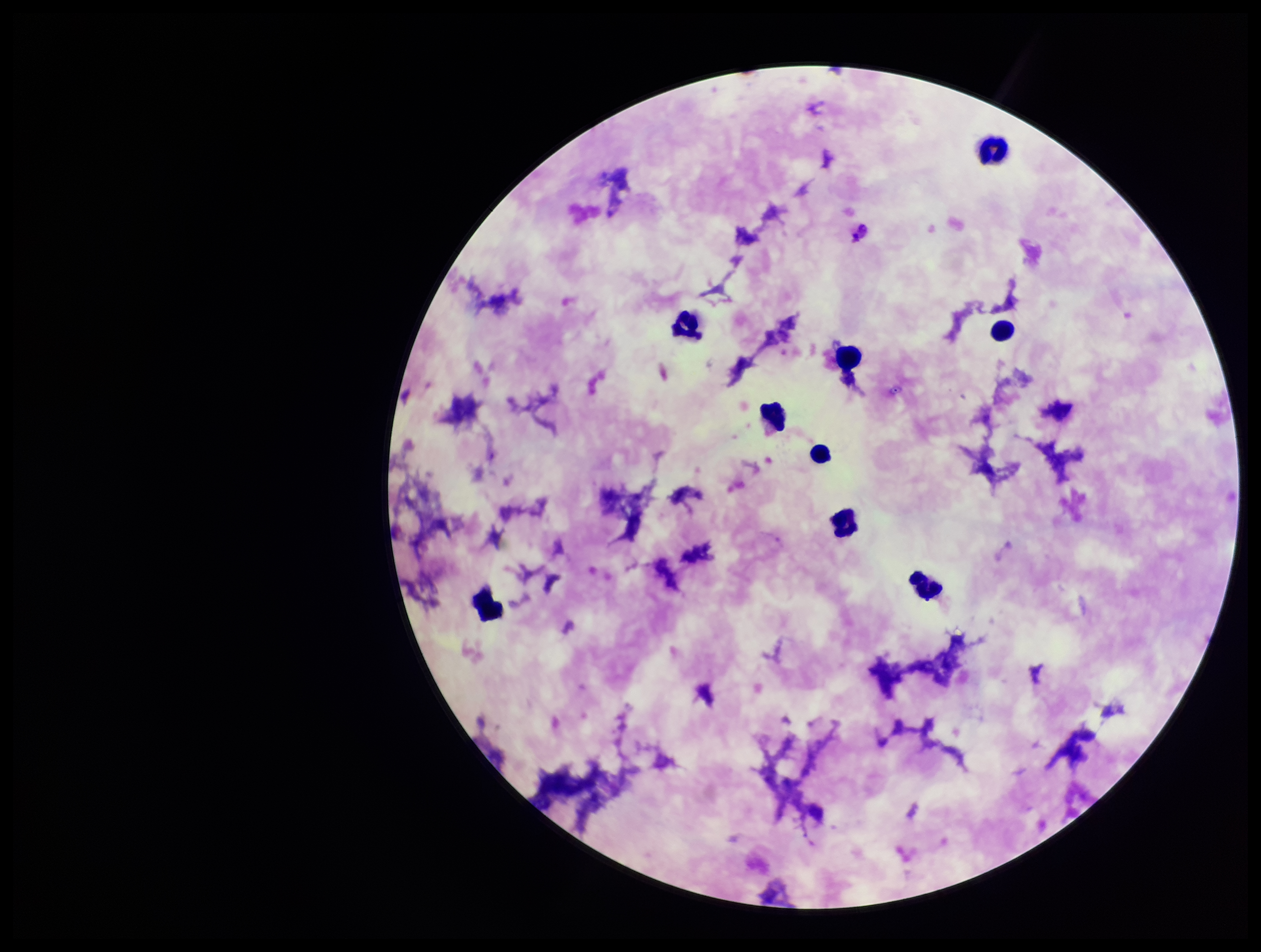
stain = Giemsa
preparation = thick blood smear
field of view = single
patient malaria status = positive
leukocyte count = 9
species reported for this patient = Plasmodium falciparum
capture = smartphone photograph through the microscope eyepiece
parasite count = 0
Plasmodium parasites = none identified
image size = 1261×952 pixels